Locate every Plasmodium vivax-infected red blood cell.
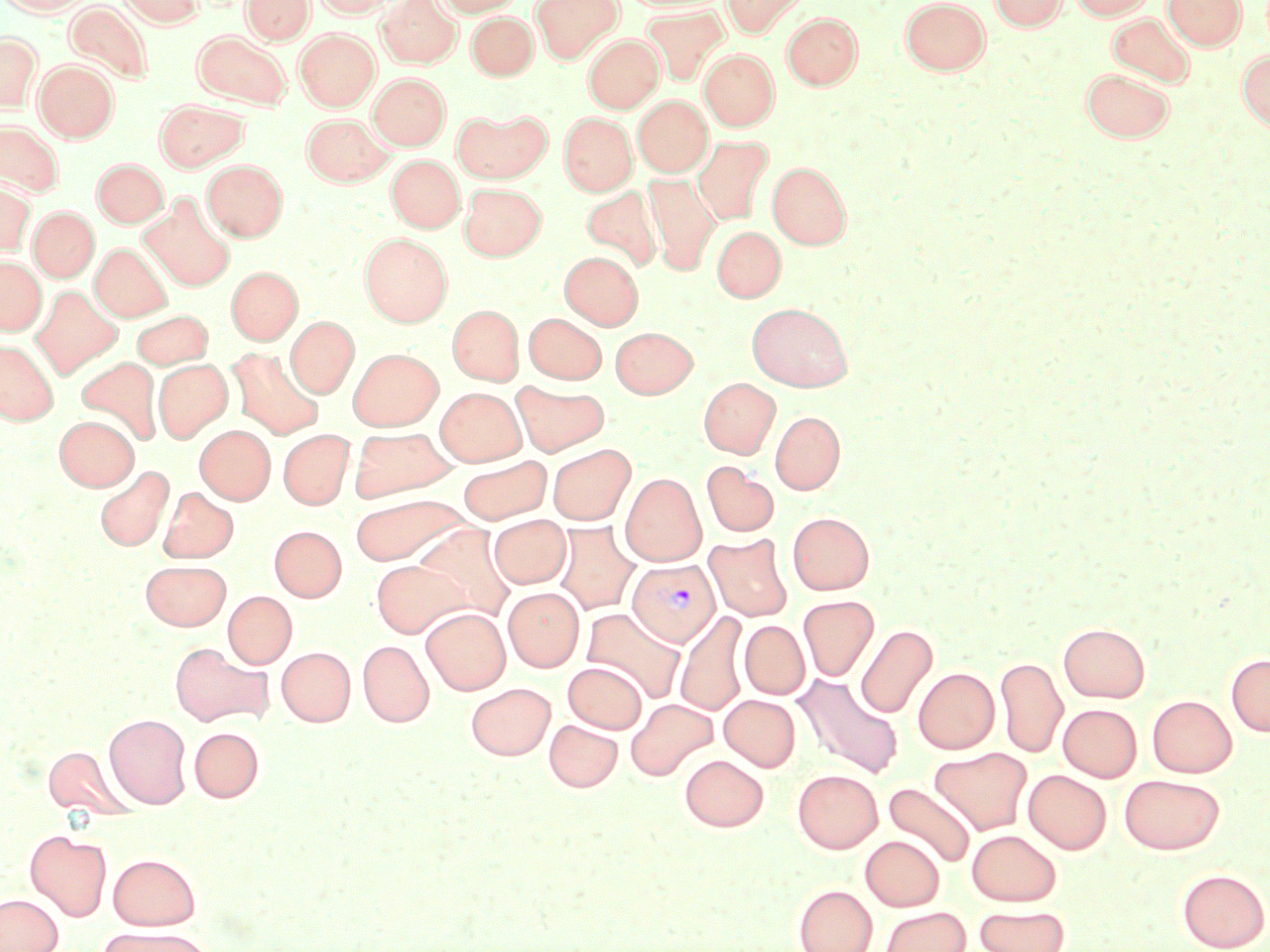
Approximate bounding boxes as (x1,y1)-(x2,y2) corner pairs in pixels.
Plasmodium vivax-infected red blood cells: (627,559)-(719,647).

{
  "slide_level_diagnosis": "Plasmodium vivax",
  "stain": "May-Grünwald-Giemsa",
  "preparation": "thin blood smear",
  "field_of_view": "single",
  "modality": "light microscopy",
  "image_size": "1270×952 pixels",
  "magnification": "1000x",
  "uninfected_red_blood_cell_locations": "approximate bounding boxes as (x1,y1)-(x2,y2) corner pairs in pixels: (1,0)-(91,15), (119,0)-(204,27), (242,0)-(314,44), (314,0)-(396,18), (376,0)-(462,69), (435,0)-(522,16), (531,0)-(622,62), (721,0)-(807,37), (901,0)-(990,74), (989,0)-(1068,31), (1069,0)-(1154,20), (1163,0)-(1246,51), (64,1)-(154,86), (642,7)-(729,86), (466,11)-(538,80), (783,13)-(863,89), (1107,13)-(1195,87), (295,29)-(380,110), (192,31)-(291,110), (0,32)-(40,110), (584,34)-(664,112), (699,49)-(779,130), (1237,51)-(1270,133), (34,60)-(118,142), (1081,69)-(1175,142), (369,73)-(449,149), (633,96)-(712,176), (155,99)-(248,171), (453,108)-(551,183), (560,112)-(636,195), (302,113)-(393,186), (0,119)-(64,197), (693,135)-(773,226), (387,155)-(464,232), (92,159)-(168,227), (202,160)-(287,241), (767,162)-(851,249), (643,174)-(720,274), (0,179)-(35,255), (459,183)-(546,260), (581,186)-(662,272), (143,193)-(236,292), (29,207)-(99,282), (711,225)-(785,302), (360,233)-(452,326), (90,243)-(172,322), (560,251)-(642,329), (0,257)-(46,335), (227,266)-(302,344), (31,286)-(122,379), (746,302)-(853,391), (448,305)-(523,385), (130,310)-(212,370), (524,313)-(607,384), (286,316)-(358,398), (611,327)-(697,398), (0,340)-(57,424), (228,348)-(324,439), (348,348)-(443,430), (76,357)-(161,446), (153,359)-(232,442), (699,377)-(780,458), (511,381)-(609,456), (435,387)-(526,466), (770,411)-(845,494), (55,415)-(138,490), (195,425)-(274,503), (347,426)-(460,503), (278,429)-(354,509), (548,444)-(635,524), (459,454)-(553,524), (701,461)-(779,537), (95,465)-(174,551), (621,473)-(706,566), (158,487)-(238,562), (349,493)-(472,565), (787,512)-(874,594), (488,515)-(572,589), (553,522)-(640,615), (413,523)-(518,621), (270,525)-(346,601), (704,533)-(793,621), (141,560)-(231,629), (371,560)-(470,638), (503,587)-(584,672), (223,591)-(296,668), (798,595)-(879,681), (422,607)-(510,695), (582,607)-(688,704), (675,611)-(750,716), (739,620)-(810,699), (1059,623)-(1149,702), (855,624)-(937,718), (358,640)-(434,726), (170,642)-(272,727), (277,647)-(355,726), (1226,653)-(1270,736), (995,656)-(1068,758), (564,661)-(647,733), (913,667)-(999,754), (794,673)-(904,778), (466,682)-(555,760), (720,694)-(800,771), (1147,695)-(1237,777), (626,698)-(718,781), (1058,703)-(1142,781), (104,713)-(192,808), (544,719)-(622,791), (189,727)-(264,802), (43,745)-(133,821), (930,747)-(1033,835), (680,754)-(768,831), (793,769)-(883,853), (1024,770)-(1111,853), (1120,774)-(1225,854), (883,783)-(977,868), (25,829)-(112,921), (967,829)-(1061,905), (861,835)-(944,910), (108,853)-(201,930), (1177,869)-(1269,951), (793,885)-(877,952), (0,894)-(62,952), (974,905)-(1070,952), (880,907)-(970,952), (98,926)-(217,952)"
}